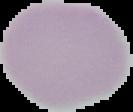
Summary:
  - Image size: 133×112 pixels
  - Image type: cell region segmented out of the field of view; surrounding area masked to black
  - Malaria status: uninfected
  - Preparation: thin blood film